Assess this cell for malaria.
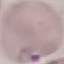

It is parasitized.

Acquired by smartphone through the microscope eyepiece. Automatically extracted cell patch, resized to 64 × 64 pixels. Thin smear of blood. Giemsa stain.